State which parasite is depicted.
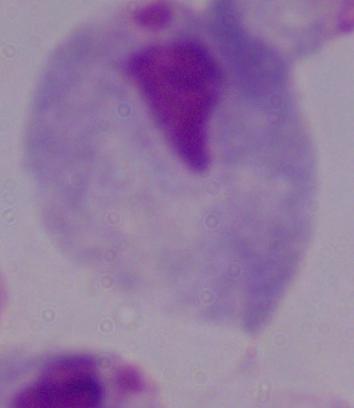

This is a trichomonad.

Summary:
  - Magnification: 1000x
  - Modality: photomicrograph